Report the malaria status of this cell.
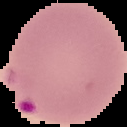

Parasitized.

image type = segmented cell region with the area outside set to black
image size = 127×127 pixels
preparation = thin blood smear